Evaluate for malaria.
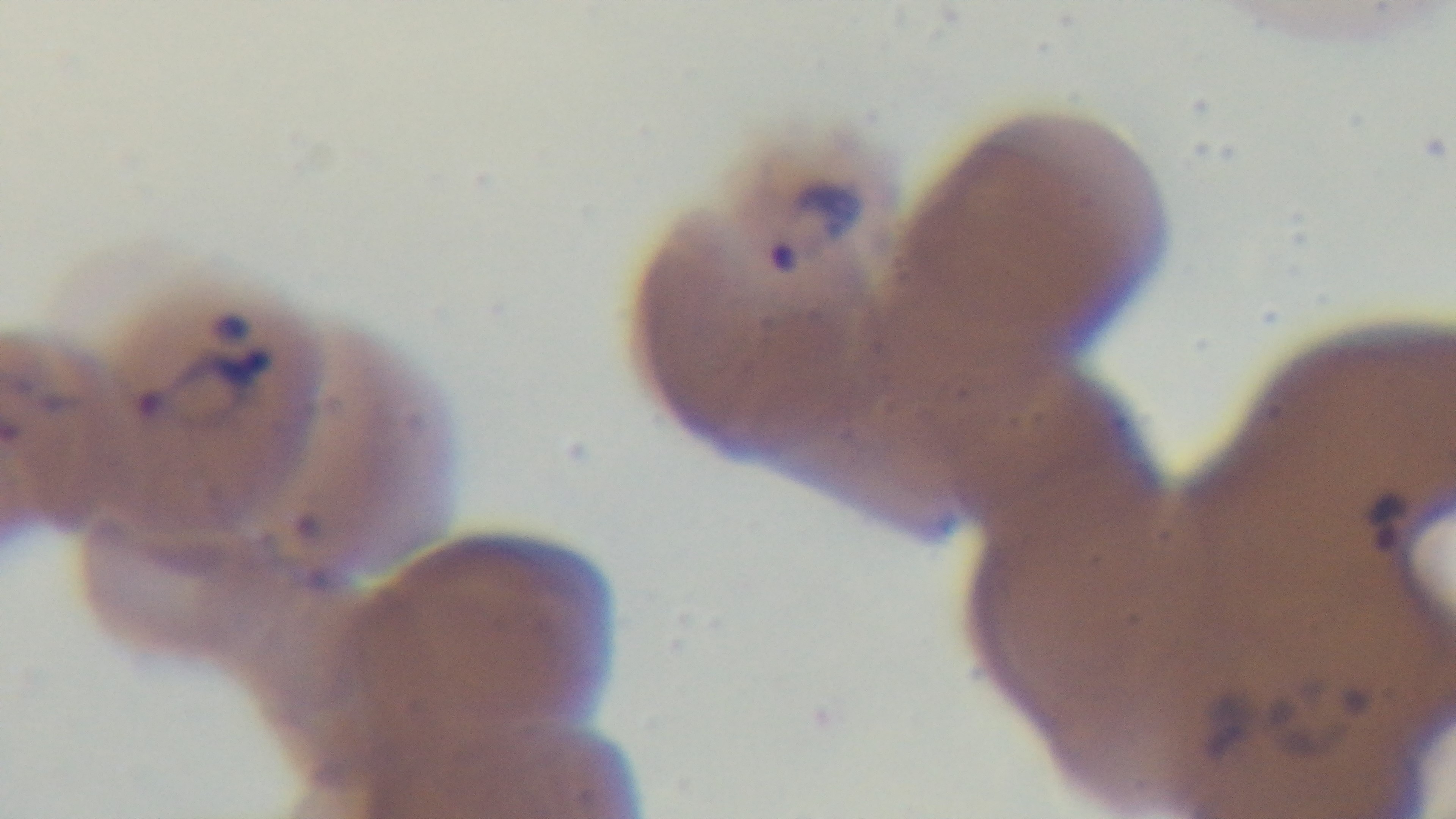

Infected.

Giemsa-stained. Photomicrograph. Preparation: thin blood film. Mounted 4K digital camera. 100x oil-immersion objective. One field from the slide.